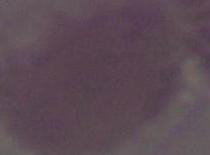

magnification = 1000x
identification = red blood cell
modality = photomicrograph